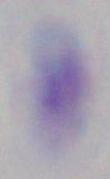

1000x magnification. Micrograph. Toxoplasma gondii is shown.